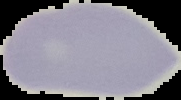

Summary:
  - Image type: segmented cell region on a black background
  - Preparation: thin blood smear
  - Malaria status: uninfected
  - Image size: 181×100 pixels